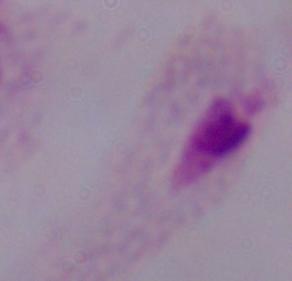 1000x magnification. A trichomonad is seen. Micrograph.